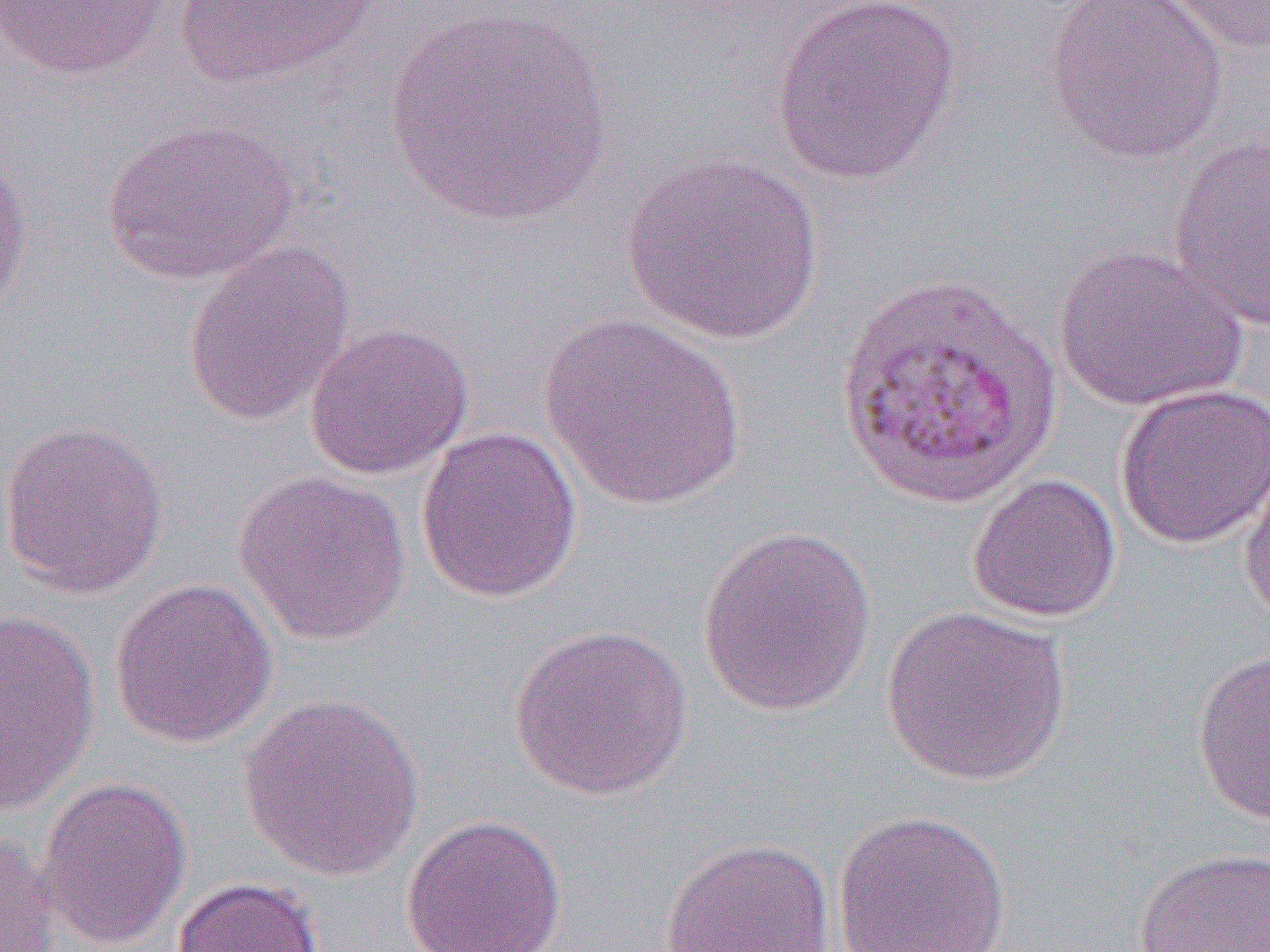 Approximate bounding boxes as (x1, y1, x2, y2) in pixels. Uninfected red blood cell locations: (0, 0, 172, 81), (169, 0, 388, 90), (771, 0, 961, 185), (1042, 0, 1230, 167), (1158, 0, 1270, 53), (384, 4, 614, 228), (100, 118, 299, 286), (1167, 133, 1270, 331), (0, 153, 33, 331), (620, 153, 824, 345), (182, 241, 355, 427), (1051, 244, 1250, 414), (536, 313, 748, 511), (304, 321, 474, 481), (1114, 383, 1270, 550), (0, 419, 169, 599), (416, 426, 583, 604), (1238, 457, 1270, 628), (233, 470, 412, 646), (966, 474, 1122, 623), (697, 525, 877, 718), (108, 576, 278, 748), (880, 605, 1071, 786), (0, 609, 100, 814), (508, 624, 694, 801), (1192, 649, 1270, 828), (237, 692, 426, 881), (36, 776, 193, 951), (833, 809, 1012, 952), (400, 813, 568, 952), (0, 830, 64, 952), (660, 836, 837, 951), (1134, 847, 1270, 951), (172, 876, 324, 952). Slide-level diagnosis: Plasmodium vivax. One field of a larger specimen. Thin blood smear. Image is 1270×952 pixels. Optical microscopy. Captured at 1000x magnification.